Identify the parasite.
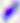
This is Toxoplasma gondii.

Summary:
  - Magnification: 400x
  - Modality: micrograph